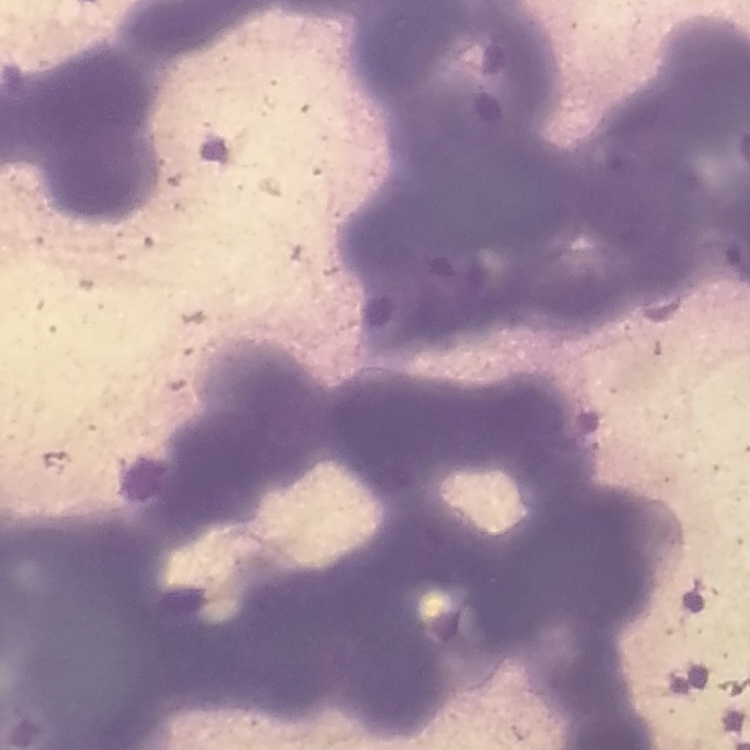
red blood cell morphology = rouleaux formation
stain = Field's or Giemsa
preparation = thin peripheral smear
image type = one tile cut from a larger photomicrograph